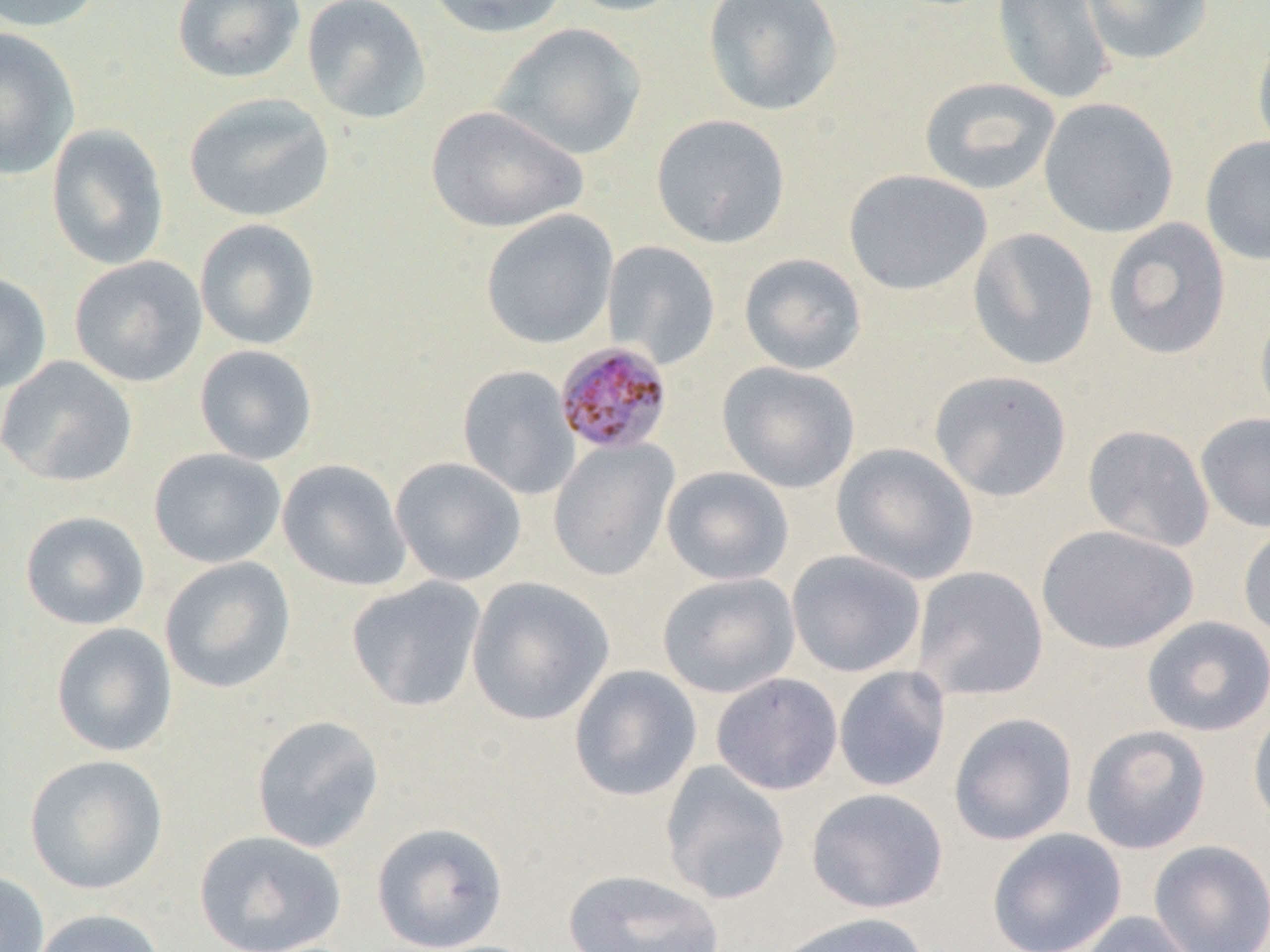
slide-level diagnosis = Plasmodium malariae
preparation = thin blood smear
uninfected red blood cell locations = approximate bounding boxes as (x1,y1)-(x2,y2) corner pairs in pixels: (0,0)-(106,33), (171,0)-(306,85), (301,0)-(431,124), (424,0)-(569,39), (563,0)-(693,17), (702,0)-(843,117), (991,0)-(1115,106), (1081,0)-(1212,66), (492,23)-(647,161), (0,28)-(80,180), (1252,31)-(1270,162), (918,77)-(1061,196), (183,92)-(335,223), (1038,97)-(1179,238), (426,105)-(588,234), (650,113)-(791,248), (46,124)-(170,270), (1200,135)-(1270,267), (843,169)-(992,296), (481,210)-(618,349), (1103,217)-(1232,360), (194,218)-(321,350), (968,227)-(1099,370), (602,240)-(721,369), (739,253)-(867,375), (69,255)-(207,388), (0,271)-(52,395), (1254,302)-(1270,430), (194,344)-(318,466), (0,355)-(137,487), (717,361)-(861,493), (457,365)-(581,500), (929,370)-(1073,503), (1195,412)-(1270,533), (1082,424)-(1215,553), (548,438)-(679,581), (831,442)-(979,585), (148,448)-(286,569), (390,457)-(527,586), (277,459)-(412,592), (661,466)-(795,586), (20,510)-(150,631), (1036,524)-(1198,655), (1238,524)-(1270,642), (786,550)-(926,677), (160,556)-(296,694), (912,566)-(1049,701), (657,572)-(801,698), (346,577)-(487,712), (466,577)-(614,726), (1141,616)-(1270,736), (51,622)-(178,757), (569,665)-(702,802), (833,665)-(951,792), (711,673)-(843,795), (1248,705)-(1270,831), (948,711)-(1079,846), (251,715)-(385,853), (1081,724)-(1212,854), (24,754)-(168,895), (659,761)-(792,905), (806,788)-(949,913), (371,822)-(508,951), (986,828)-(1127,952), (193,830)-(347,952), (1148,840)-(1270,952), (561,869)-(725,952), (0,870)-(50,952), (29,908)-(167,952), (1076,911)-(1201,952), (772,912)-(931,952)
image size = 1270×952 pixels
field of view = single
magnification = 1000x
Plasmodium malariae-infected red blood cell locations = approximate bounding boxes as (x1,y1)-(x2,y2) corner pairs in pixels: (555,342)-(674,455)
modality = optical microscopy